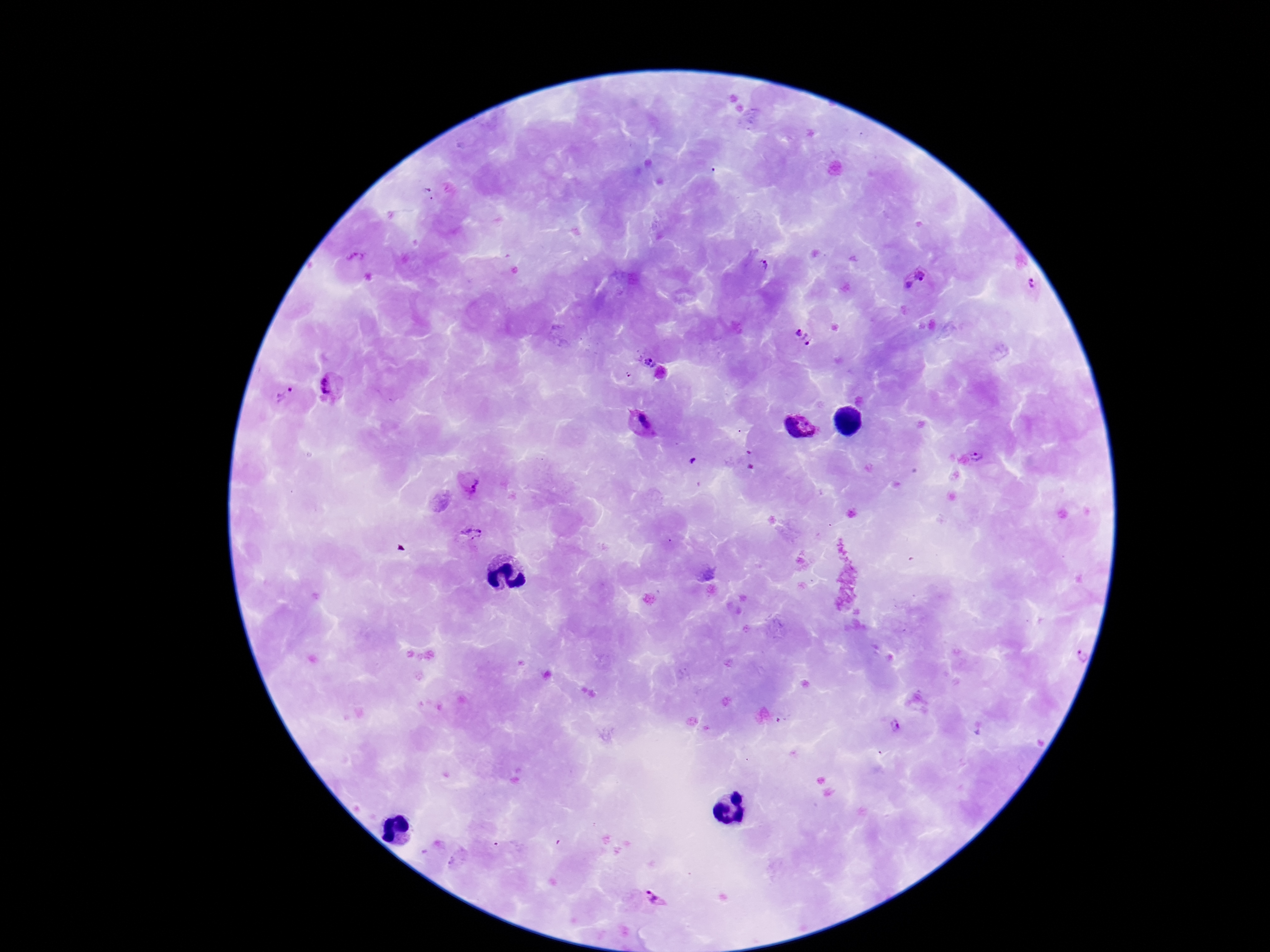
magnification = 100x
field of view = one from this slide
patient malaria status = infected
capture = smartphone camera through the microscope eyepiece
Plasmodium parasite locations = approximate centers as (x, y) in pixels: (427, 193), (357, 258), (759, 268), (919, 281), (1031, 283), (804, 337), (650, 362), (629, 375), (330, 388), (282, 394), (641, 424), (800, 428), (981, 456), (694, 459), (469, 483), (469, 536), (896, 727), (457, 861), (656, 899)
preparation = thick peripheral-blood smear
image size = 1270×952 pixels
stain = Giemsa